Assess this cell for malaria.
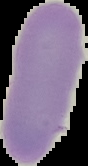
It is uninfected.

Summary:
  - Preparation: thin blood film
  - Image size: 88×166 pixels
  - Image type: segmented cell region with the area outside set to black